Assess this cell for malaria.
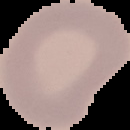

It is uninfected.

From a thin blood smear. The area outside the segmented cell region is set to black. Image is 130×130 pixels.